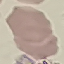

Summary:
  - Malaria status: uninfected
  - Stain: Giemsa
  - Capture: smartphone camera at the microscope eyepiece
  - Image type: cell patch, automatically extracted from a larger field of view and resized to 64 × 64 pixels
  - Preparation: thin blood film